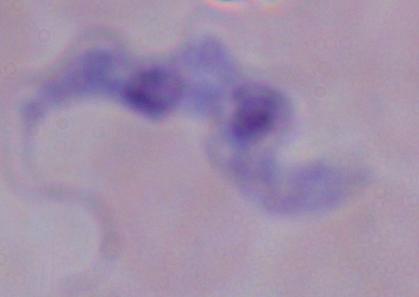

Summary:
  - Magnification: 1000x
  - Identification: trypanosome
  - Modality: photomicrograph